Assess this cell for malaria.
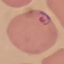
It is parasitized.

Thin smear of blood. Cell patch, automatically extracted from a larger field of view and resized to 64 × 64 pixels. Giemsa-stained preparation. Acquired by smartphone through the microscope eyepiece.